Locate every blood parasite and identify its species.
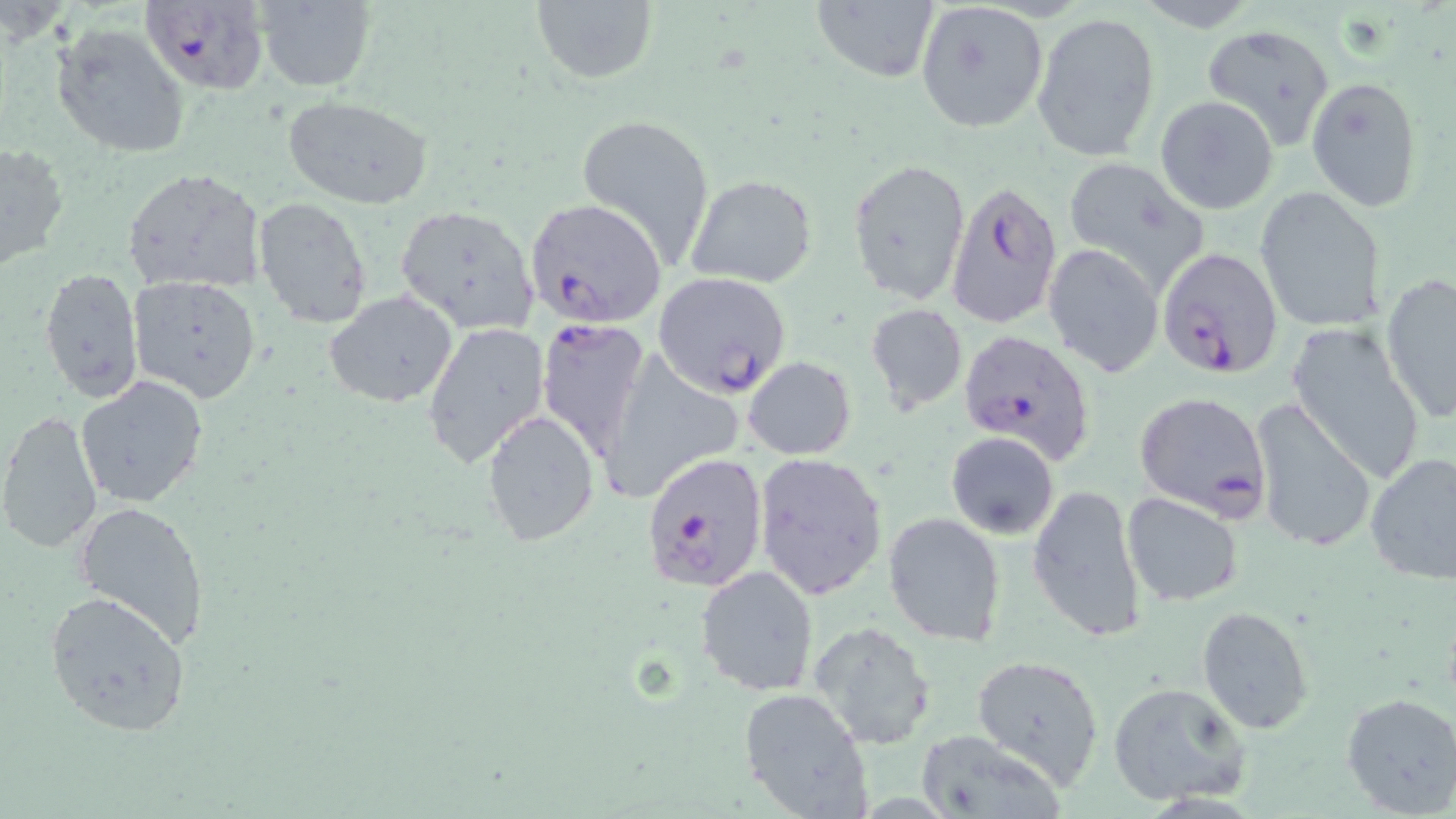

Approximate bounding boxes as (x1, y1, x2, y2) in pixels.
Plasmodium falciparum-infected red blood cells: (142, 1, 270, 95), (945, 179, 1064, 331), (525, 198, 667, 328), (1158, 246, 1285, 379), (652, 271, 792, 397), (534, 318, 651, 461), (956, 328, 1097, 464), (1134, 392, 1272, 516), (642, 452, 768, 590).
No Plasmodium ovale, Plasmodium malariae, Plasmodium vivax, Babesia divergens, or Trypanosoma brucei observed.

Uninfected red blood cell locations: (257, 0, 376, 92), (530, 1, 658, 86), (812, 1, 941, 83), (915, 2, 1050, 134), (1032, 11, 1161, 164), (1200, 23, 1337, 150), (51, 24, 189, 160), (1307, 76, 1426, 214), (281, 95, 433, 208), (1155, 95, 1279, 214), (575, 112, 716, 267), (1, 139, 70, 272), (847, 157, 970, 306), (1061, 157, 1212, 288), (121, 167, 267, 296), (686, 173, 817, 288), (1255, 185, 1385, 332), (252, 198, 373, 330), (395, 205, 540, 334), (1043, 244, 1163, 377), (40, 267, 143, 403), (1378, 273, 1456, 421), (128, 275, 261, 403), (323, 291, 459, 408), (865, 304, 968, 413), (1286, 320, 1427, 486), (423, 322, 549, 471), (743, 356, 856, 458), (75, 375, 209, 508), (1250, 398, 1377, 553), (481, 408, 600, 546), (0, 410, 103, 554), (945, 431, 1059, 538), (752, 450, 888, 600), (1364, 450, 1456, 591), (1027, 483, 1148, 642), (1122, 492, 1246, 607), (72, 498, 212, 650), (882, 512, 1005, 648), (696, 564, 820, 698), (43, 590, 192, 737), (1196, 606, 1317, 735), (808, 620, 938, 749), (971, 654, 1105, 788), (1107, 682, 1252, 807), (737, 688, 870, 818), (1340, 691, 1456, 816), (917, 731, 1064, 819). Slide-level diagnosis: Plasmodium falciparum. May-Grünwald-Giemsa stain. Captured at 1000x magnification. Light microscopy. One field of a larger specimen. Image is 1456×819 pixels. Thin blood smear.